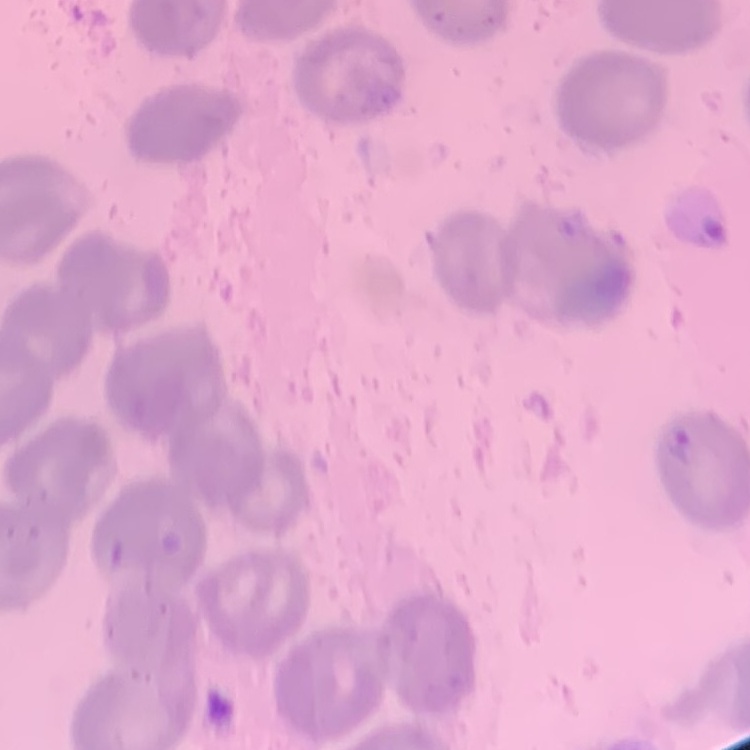
{
  "red_blood_cell_morphology": "no rouleaux formation",
  "preparation": "thin peripheral smear",
  "stain": "Field's or Giemsa",
  "image_type": "one tile cut from a larger photomicrograph"
}